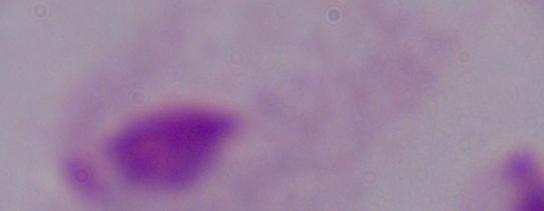
modality = micrograph
magnification = 1000x
identification = trichomonad